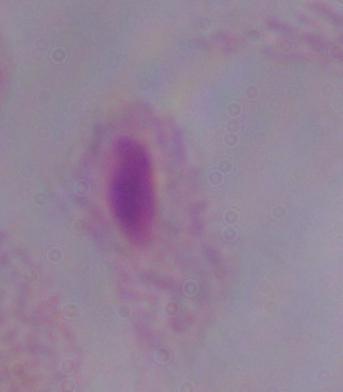

A trichomonad is shown. Photomicrograph. 1000x magnification.